Give the preparation type.
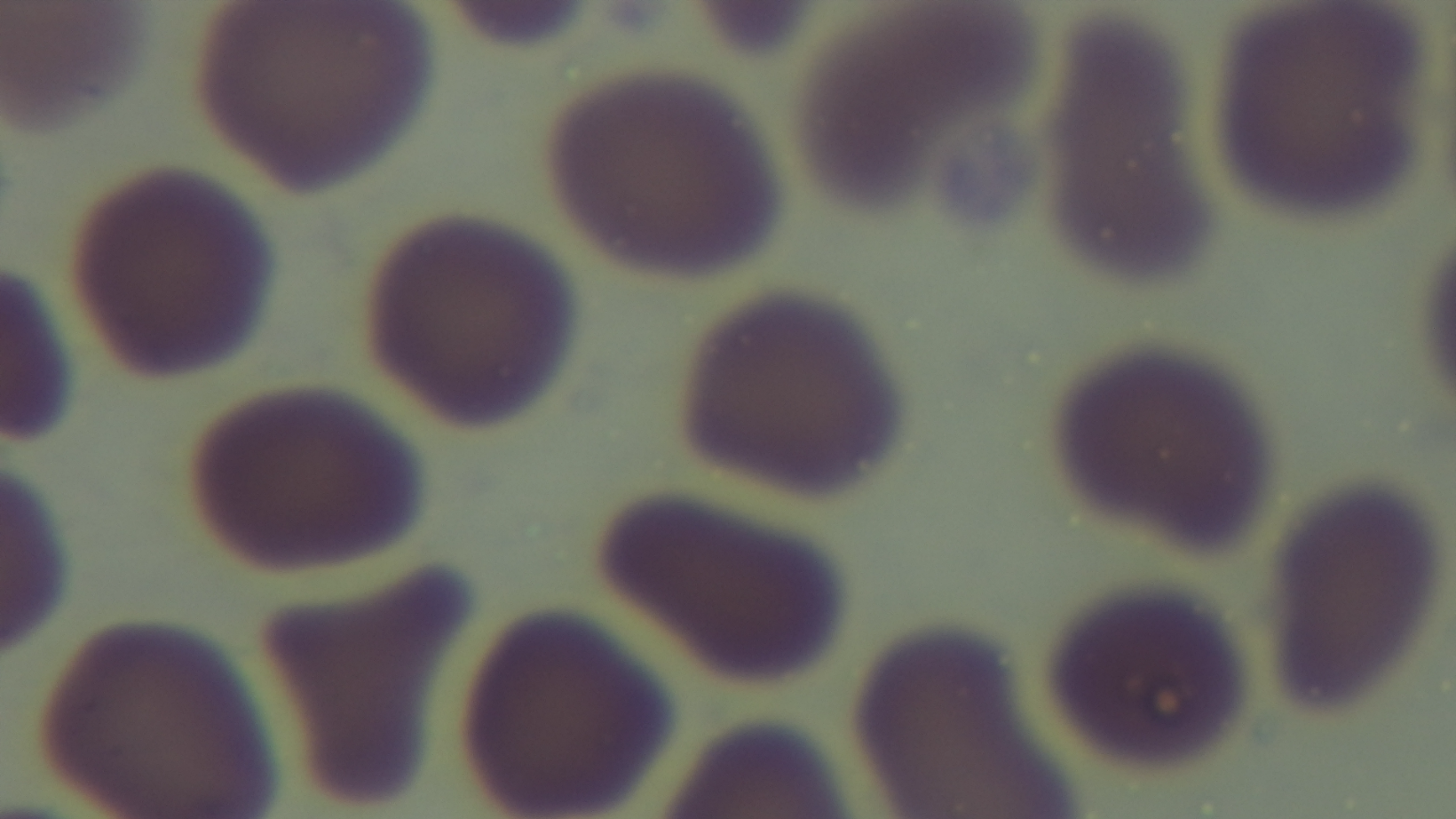
It is a thin blood film.

Photomicrograph. One field from the slide. Malaria status: negative. Captured with a mounted 4K digital camera. Oil-immersion objective, 100x. Giemsa-stained.